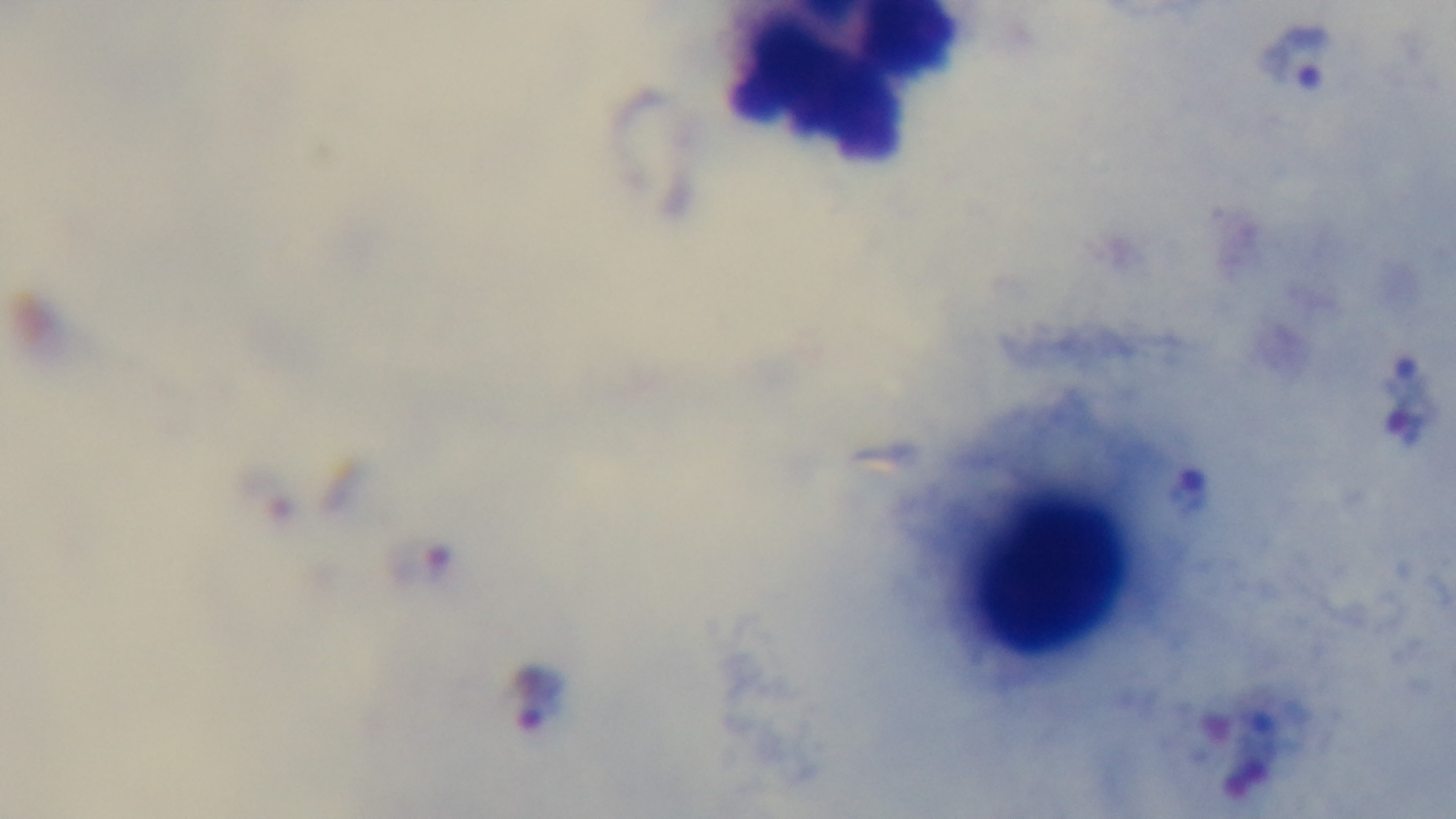
Preparation: thick smear. Malaria status: infected. Giemsa stain. Oil-immersion objective, 100x. One field from the slide. Photomicrograph. Mounted 4K digital camera.